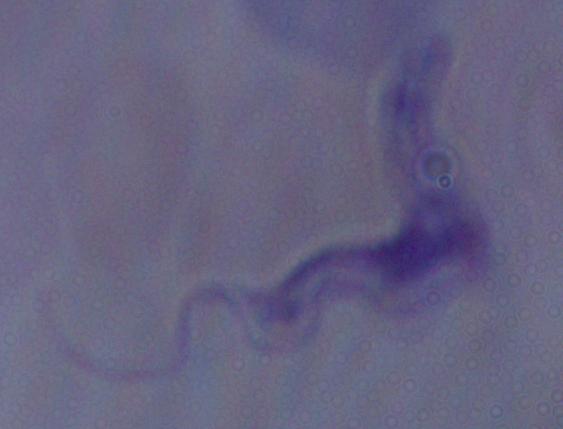

magnification = 1000x
modality = micrograph
identification = trypanosome